Assess this cell for malaria.
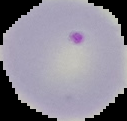
Parasitized.

Summary:
  - Image type: segmented cell region on a black background
  - Preparation: thin blood smear
  - Image size: 127×121 pixels